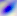
Summary:
  - Magnification: 400x
  - Modality: micrograph
  - Identification: Toxoplasma gondii